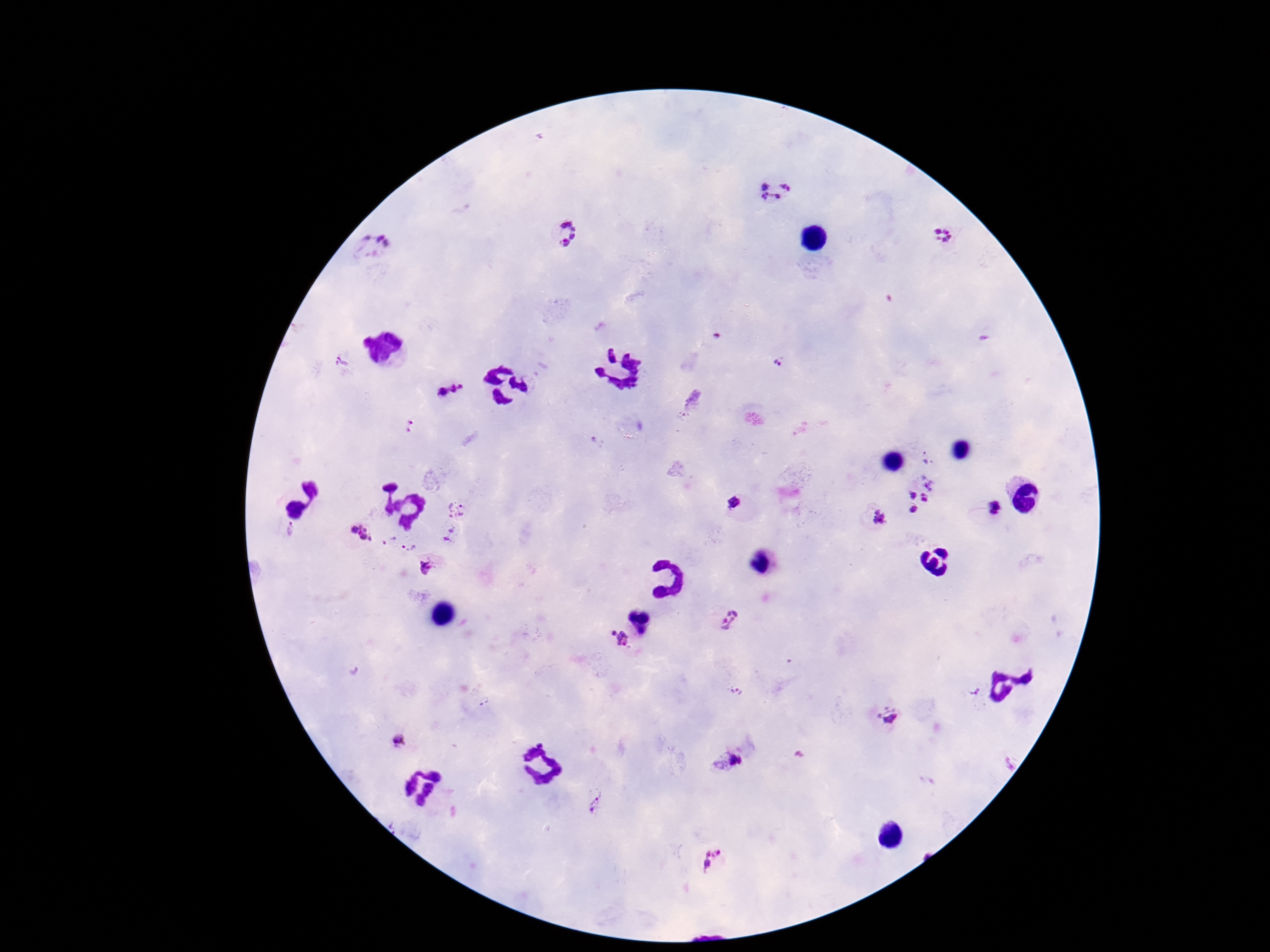

Approximate centers as (x, y) in pixels.
Summary:
  - Plasmodium parasite locations: (774, 191), (564, 235), (944, 236), (375, 248), (778, 359), (341, 363), (449, 390), (693, 397), (408, 425), (598, 444), (932, 480), (911, 495), (923, 496), (734, 502), (998, 507), (457, 508), (915, 510), (878, 517), (289, 530), (360, 533), (449, 535), (389, 540), (410, 544), (428, 568), (728, 618), (623, 641), (738, 692), (886, 716), (398, 740), (727, 760), (593, 804), (713, 859)
  - Magnification: 100x
  - Preparation: thick blood smear
  - Patient malaria status: positive
  - Field of view: one from this slide
  - Capture: smartphone camera through the microscope eyepiece
  - Stain: Giemsa
  - Image size: 1270×952 pixels